Give the extent of all uninfected red blood cells.
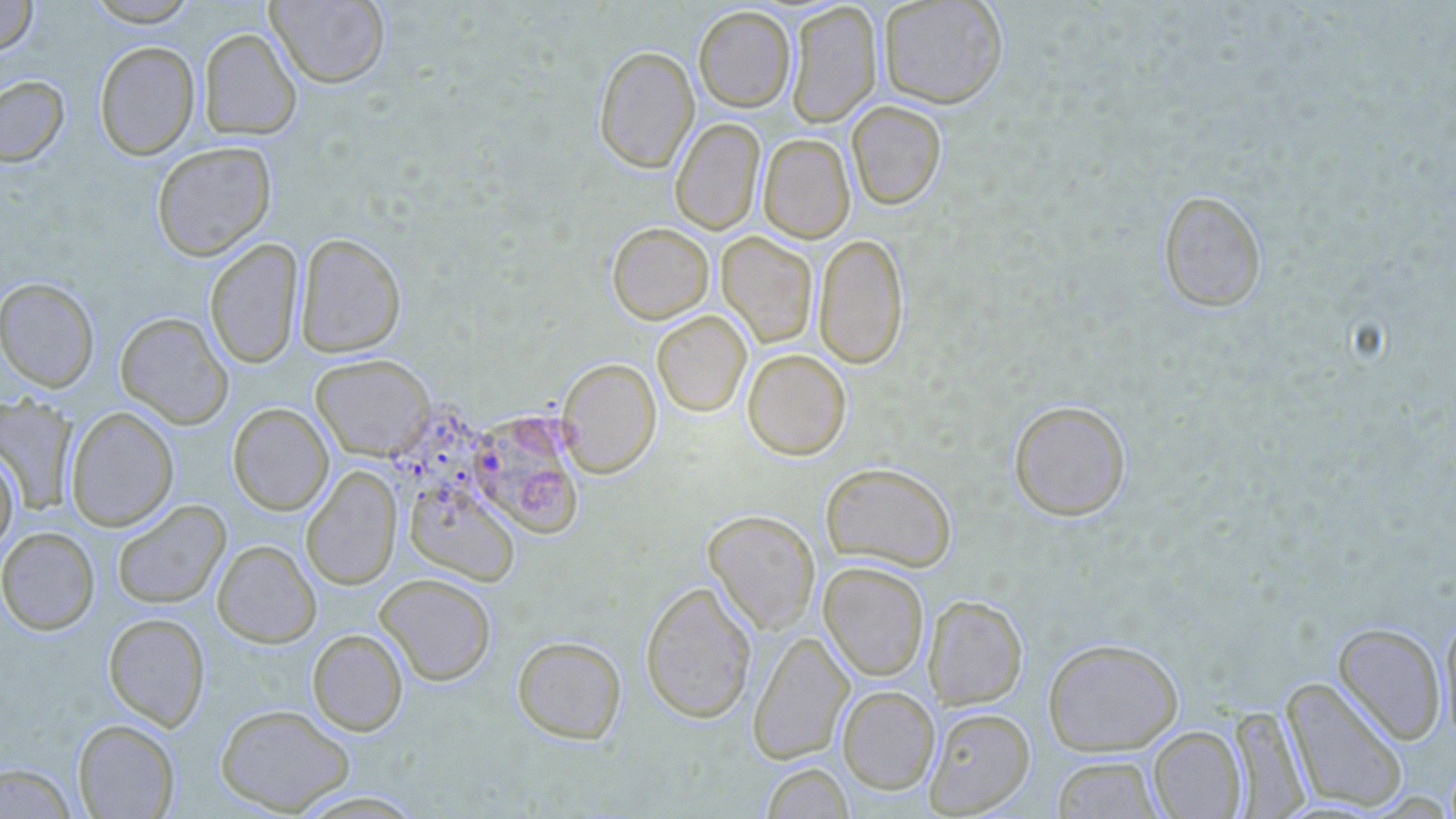

Approximate bounding boxes as [x1, y1, x2, y2] in pixels.
Uninfected red blood cells: [0, 0, 38, 55], [85, 0, 200, 26], [265, 0, 390, 88], [878, 0, 1008, 108], [785, 2, 882, 127], [693, 5, 796, 112], [198, 28, 301, 141], [94, 41, 200, 160], [593, 45, 699, 173], [0, 75, 69, 167], [846, 100, 947, 210], [670, 118, 765, 235], [758, 134, 855, 243], [151, 141, 276, 261], [1158, 189, 1267, 312], [607, 222, 714, 324], [294, 232, 406, 358], [717, 232, 817, 347], [813, 233, 909, 369], [205, 238, 303, 369], [0, 277, 100, 392], [652, 310, 752, 417], [115, 312, 233, 429], [742, 349, 852, 460], [310, 354, 435, 460], [557, 358, 661, 477], [0, 395, 79, 514], [1008, 400, 1131, 521], [227, 403, 334, 516], [65, 407, 179, 530], [468, 409, 586, 538], [0, 448, 19, 554], [820, 461, 957, 572], [301, 466, 402, 590], [405, 480, 520, 586], [112, 500, 231, 609], [702, 509, 821, 634], [0, 526, 100, 635], [211, 540, 321, 648], [818, 562, 929, 681], [374, 573, 496, 686], [640, 580, 758, 723], [923, 594, 1028, 709], [1439, 612, 1456, 748], [102, 613, 210, 730], [1333, 622, 1446, 744], [307, 629, 408, 736], [747, 630, 854, 764], [512, 636, 627, 744], [1043, 637, 1184, 756], [1281, 676, 1409, 813], [837, 686, 940, 794], [215, 703, 355, 815], [923, 706, 1036, 817], [1229, 706, 1310, 816], [73, 718, 180, 818], [1148, 726, 1246, 818], [1050, 754, 1165, 818], [0, 762, 76, 817], [761, 762, 853, 819], [290, 789, 429, 818].

slide-level diagnosis = Plasmodium falciparum
field of view = single
magnification = 1000x
image size = 1456×819 pixels
preparation = thin blood film
stain = May-Grünwald-Giemsa
modality = light microscopy